Mark where platelets are.
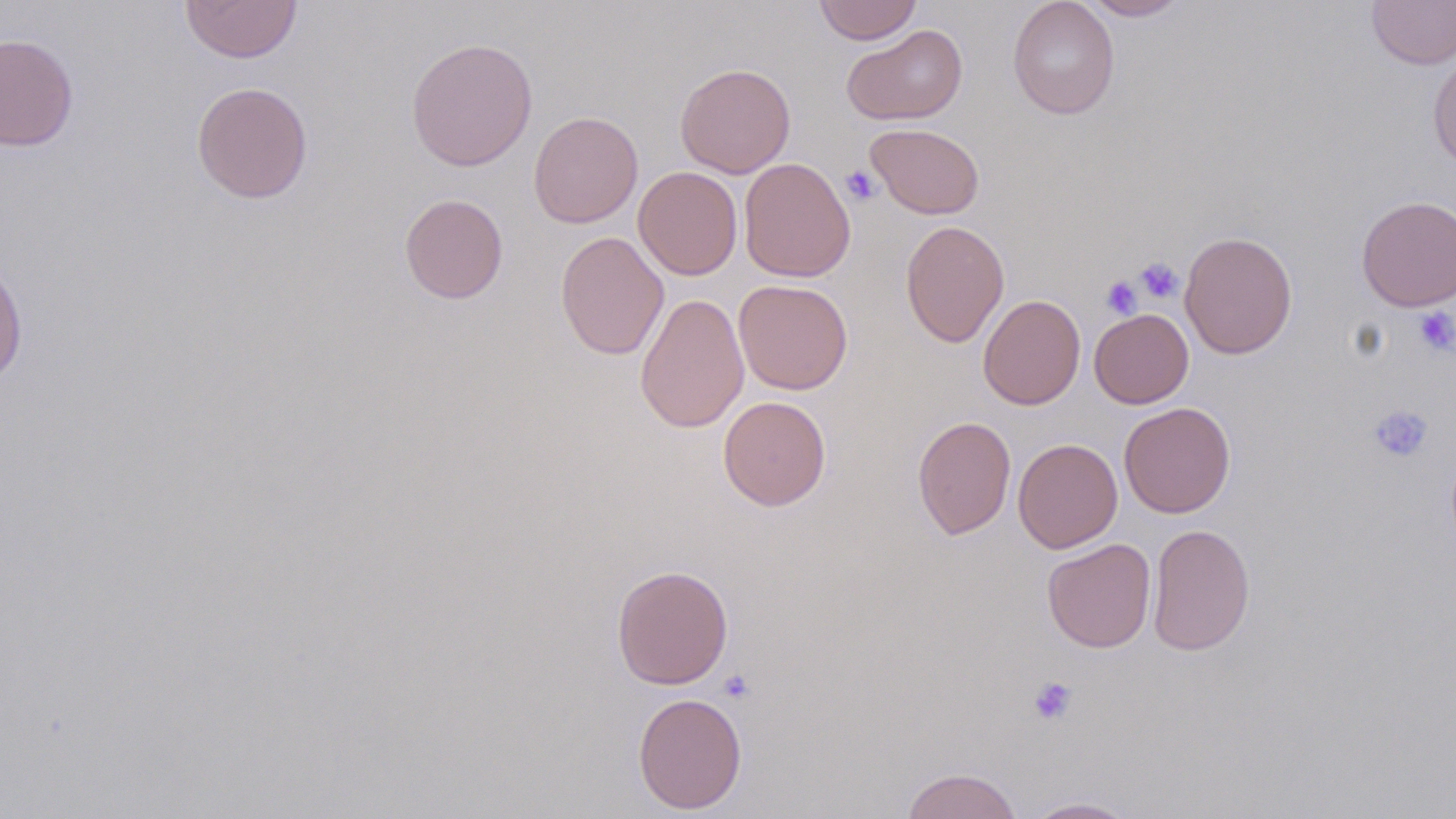

Approximate bounding boxes as (x1, y1, x2, y2) in pixels.
Platelets: (841, 165, 881, 205), (1134, 257, 1183, 304), (1100, 275, 1143, 319), (1413, 307, 1456, 356), (1368, 404, 1434, 463), (718, 669, 755, 703), (1028, 676, 1078, 725).

Summary:
  - Uninfected red blood cell locations: (180, 0, 302, 63), (813, 0, 922, 44), (1007, 0, 1120, 119), (1080, 0, 1191, 21), (1366, 0, 1456, 69), (841, 24, 968, 126), (0, 32, 79, 152), (406, 37, 538, 171), (1427, 49, 1456, 170), (674, 62, 796, 178), (191, 81, 312, 204), (528, 111, 643, 228), (865, 123, 985, 220), (738, 158, 856, 282), (633, 166, 743, 281), (398, 193, 509, 304), (1356, 195, 1455, 311), (900, 220, 1010, 348), (555, 231, 669, 360), (1179, 231, 1298, 359), (0, 255, 28, 390), (733, 279, 853, 395), (634, 292, 750, 433), (978, 295, 1086, 410), (1089, 309, 1193, 409), (718, 396, 831, 511), (1119, 402, 1236, 518), (913, 415, 1016, 540), (1013, 438, 1123, 553), (1147, 523, 1256, 656), (1042, 538, 1156, 653), (611, 564, 733, 690), (632, 692, 747, 814), (901, 767, 1024, 819), (1022, 797, 1140, 818)
  - Slide-level diagnosis: negative for blood parasites
  - Preparation: thin blood smear
  - Image size: 1456×819 pixels
  - Field of view: one of a larger specimen
  - Modality: light microscopy
  - Magnification: 1000x
  - Stain: May-Grünwald-Giemsa